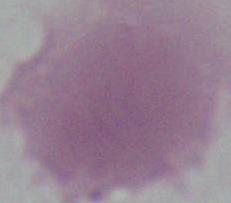

Micrograph. An erythrocyte is shown. 1000x magnification.